Identify the parasite.
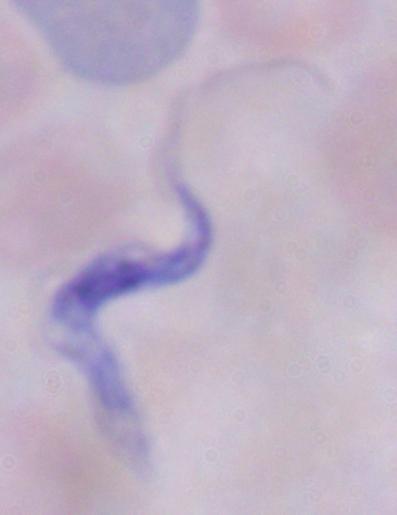
This is a trypanosome.

Summary:
  - Magnification: 1000x
  - Modality: photomicrograph